Describe the morphology of the red blood cells.
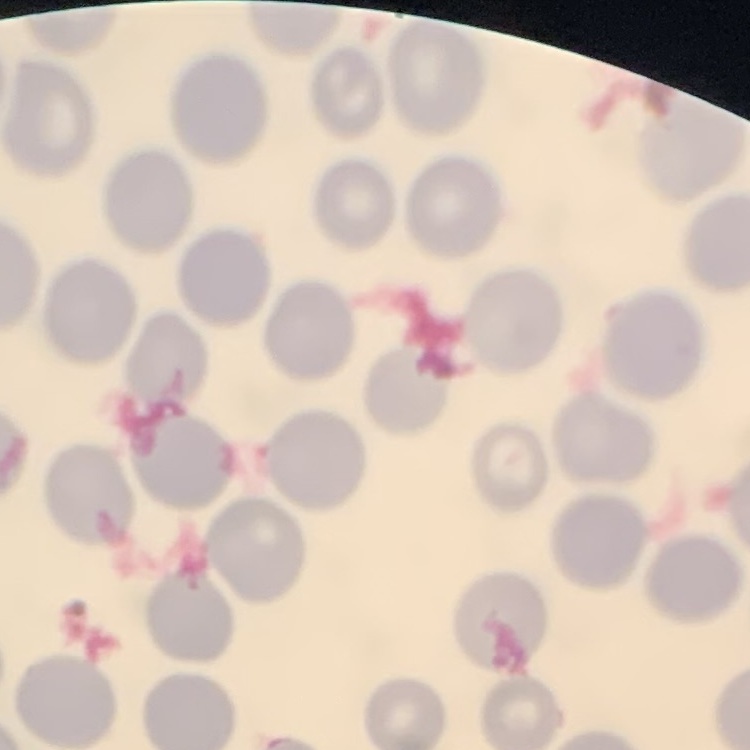
They show no rouleaux formation.

Field's or Giemsa stain. Thin blood film. Square crop of a larger photomicrograph.